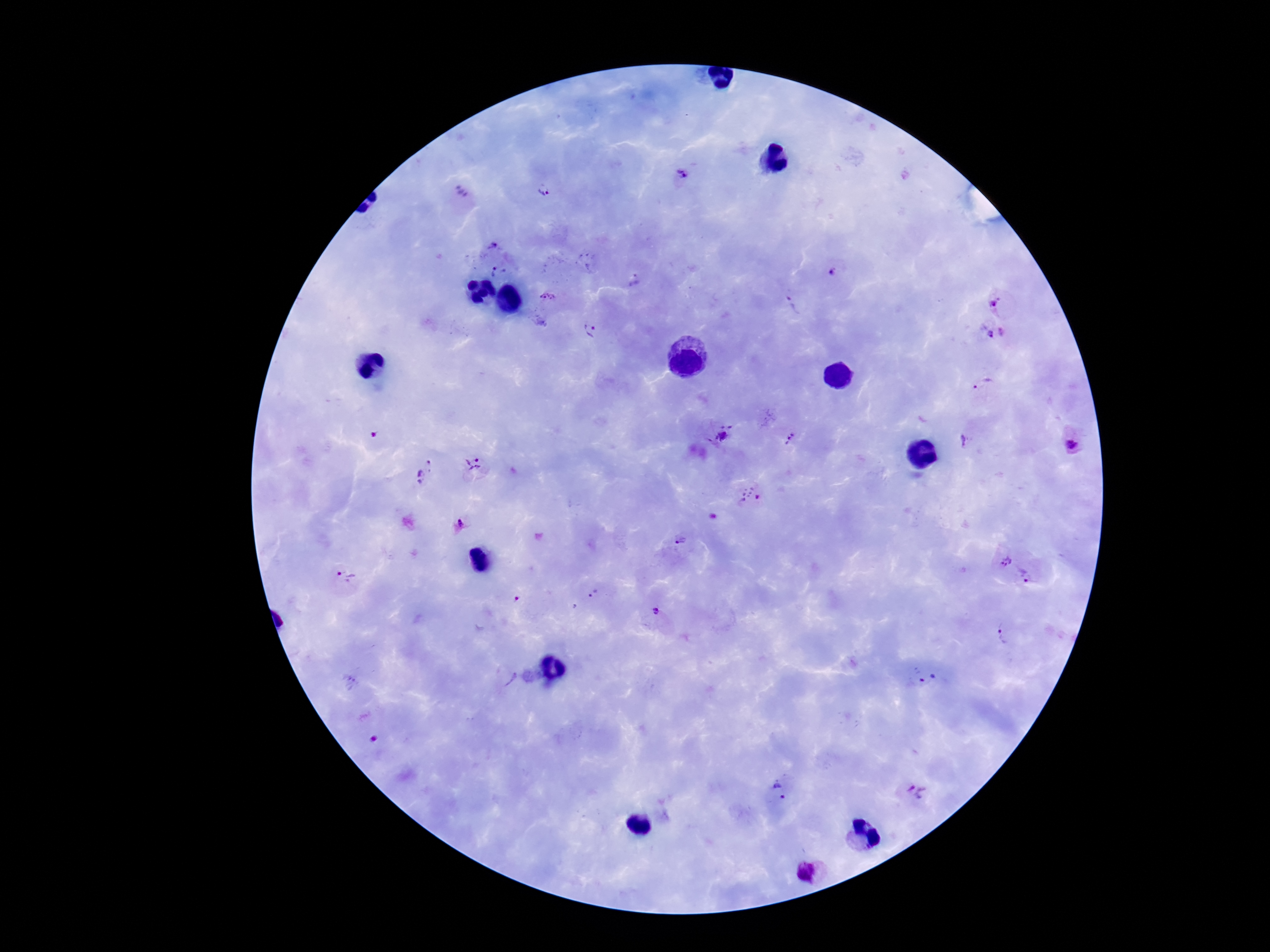
image size = 1270×952 pixels
preparation = thick peripheral-blood smear
patient malaria status = positive
Plasmodium parasite locations = approximate centers as (x, y) in pixels: (683, 174), (542, 190), (464, 193), (495, 246), (499, 273), (836, 274), (633, 280), (548, 298), (1004, 301), (792, 307), (992, 329), (588, 332), (984, 387), (723, 435), (374, 436), (789, 440), (972, 440), (1072, 445), (474, 466), (424, 471), (750, 494), (461, 525), (680, 541), (998, 558), (1030, 572), (347, 575), (596, 594), (515, 598), (657, 610), (1005, 632), (504, 676), (926, 679), (352, 682), (373, 738), (780, 790), (918, 790)
field of view = single
magnification = 100x
capture = smartphone camera through the microscope eyepiece
stain = Giemsa